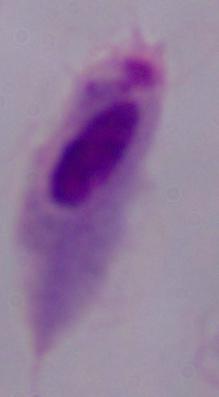
magnification = 1000x
identification = trichomonad
modality = micrograph